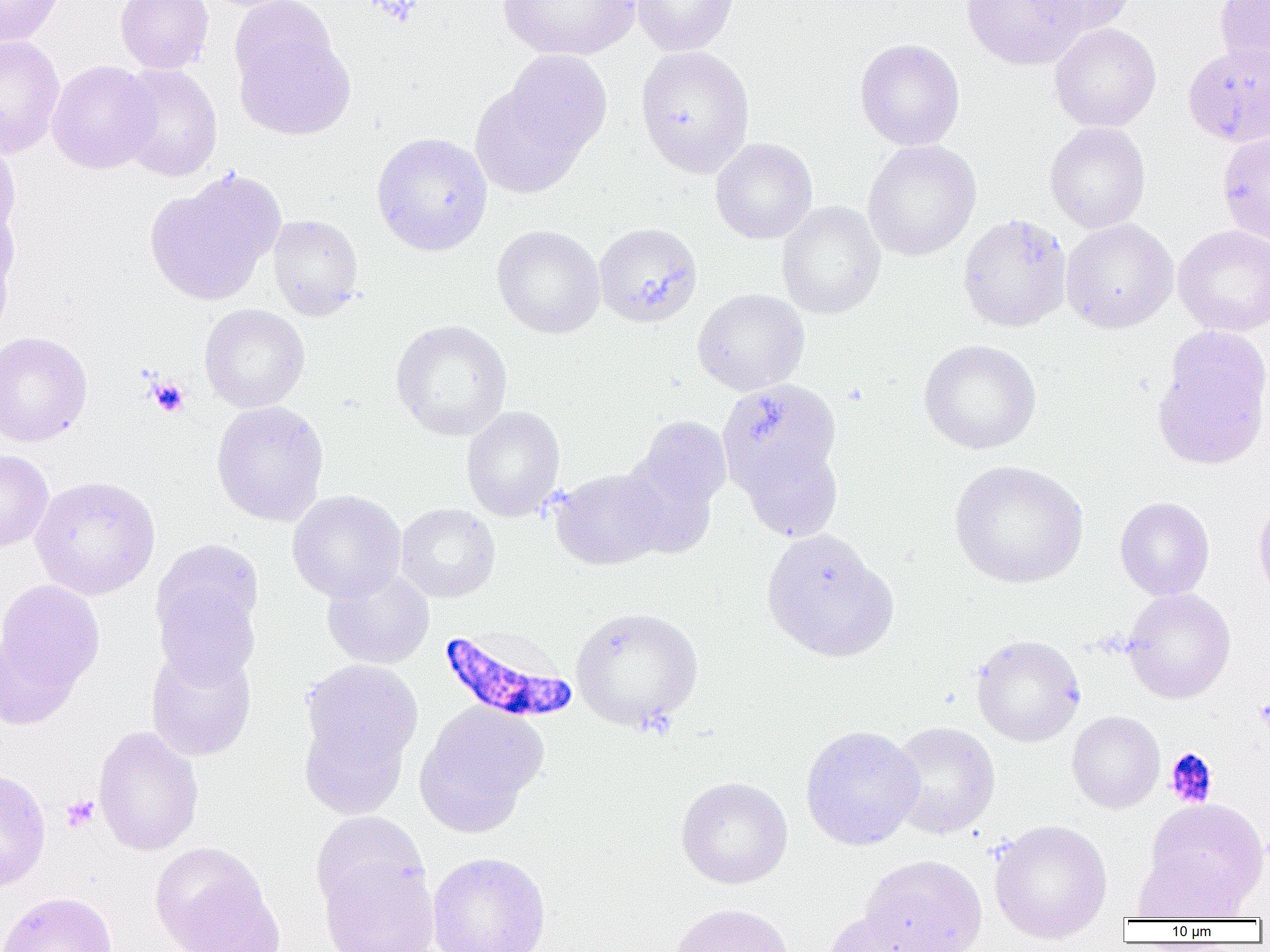

slide-level diagnosis = Plasmodium falciparum
preparation = thin blood film
Plasmodium falciparum-infected red blood cell locations = approximate bounding boxes as (x1, y1, x2, y2) in pixels: (438, 627, 579, 726)
modality = optical microscopy
magnification = 1000x
field of view = one of a larger specimen
uninfected red blood cell locations = approximate bounding boxes as (x1, y1, x2, y2) in pixels: (0, 0, 66, 46), (115, 0, 214, 73), (228, 0, 341, 98), (498, 0, 640, 61), (631, 0, 739, 56), (962, 0, 1086, 70), (1027, 0, 1136, 35), (1214, 0, 1270, 78), (1049, 23, 1161, 131), (234, 26, 355, 140), (0, 36, 65, 159), (854, 38, 965, 151), (1183, 42, 1270, 147), (635, 45, 755, 178), (47, 60, 159, 174), (115, 63, 222, 182), (472, 69, 602, 200), (1044, 122, 1151, 233), (1217, 129, 1270, 248), (371, 131, 493, 255), (0, 133, 20, 246), (710, 138, 818, 245), (862, 140, 982, 261), (144, 170, 283, 305), (0, 201, 18, 326), (776, 201, 886, 320), (958, 213, 1072, 333), (267, 214, 364, 321), (1060, 218, 1178, 333), (594, 222, 702, 328), (492, 224, 605, 338), (1173, 224, 1270, 337), (692, 288, 810, 396), (199, 304, 310, 413), (390, 319, 512, 441), (1152, 327, 1270, 470), (0, 331, 92, 447), (918, 339, 1041, 454), (720, 378, 842, 496), (210, 400, 329, 526), (461, 405, 566, 522), (621, 414, 731, 547), (741, 440, 843, 542), (0, 449, 54, 553), (948, 459, 1089, 589), (550, 469, 667, 571), (30, 475, 161, 600), (287, 490, 406, 603), (1115, 496, 1215, 600), (1253, 497, 1270, 607), (395, 503, 501, 603), (761, 529, 898, 663), (150, 541, 264, 682), (322, 566, 435, 669), (0, 578, 106, 719), (1123, 588, 1236, 704), (570, 606, 703, 732), (971, 634, 1085, 747), (145, 645, 256, 761), (300, 659, 424, 792), (414, 702, 547, 835), (1067, 710, 1165, 814), (888, 721, 1000, 839), (800, 725, 923, 851), (92, 726, 204, 857), (0, 767, 51, 894), (675, 776, 793, 889), (1145, 798, 1268, 910), (311, 811, 429, 920), (989, 819, 1112, 944), (149, 841, 282, 952), (427, 851, 552, 952), (1131, 851, 1246, 922), (859, 854, 988, 952), (318, 857, 439, 952), (0, 891, 118, 952), (669, 903, 794, 952), (821, 908, 935, 952)
image size = 1270×952 pixels
platelet locations = approximate bounding boxes as (x1, y1, x2, y2) in pixels: (147, 376, 190, 417), (1255, 693, 1270, 738), (1164, 747, 1218, 808), (61, 794, 99, 833)